Classify this cell by malaria status.
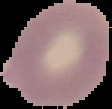

It is uninfected.

image size = 112×109 pixels
preparation = thin blood smear
image type = segmented cell region on a black background